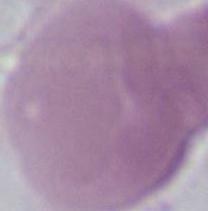 Photomicrograph. 1000x magnification. A red blood cell is shown.